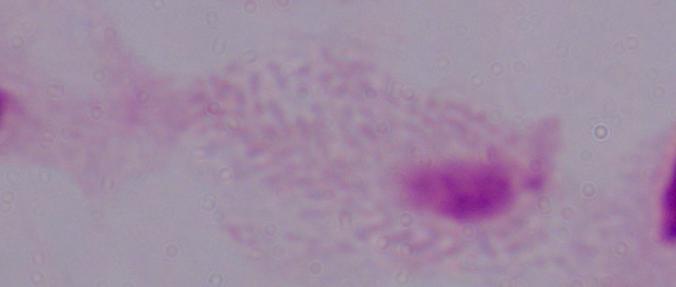
Summary:
  - Identification: trichomonad
  - Modality: photomicrograph
  - Magnification: 1000x